Name the blood parasite species.
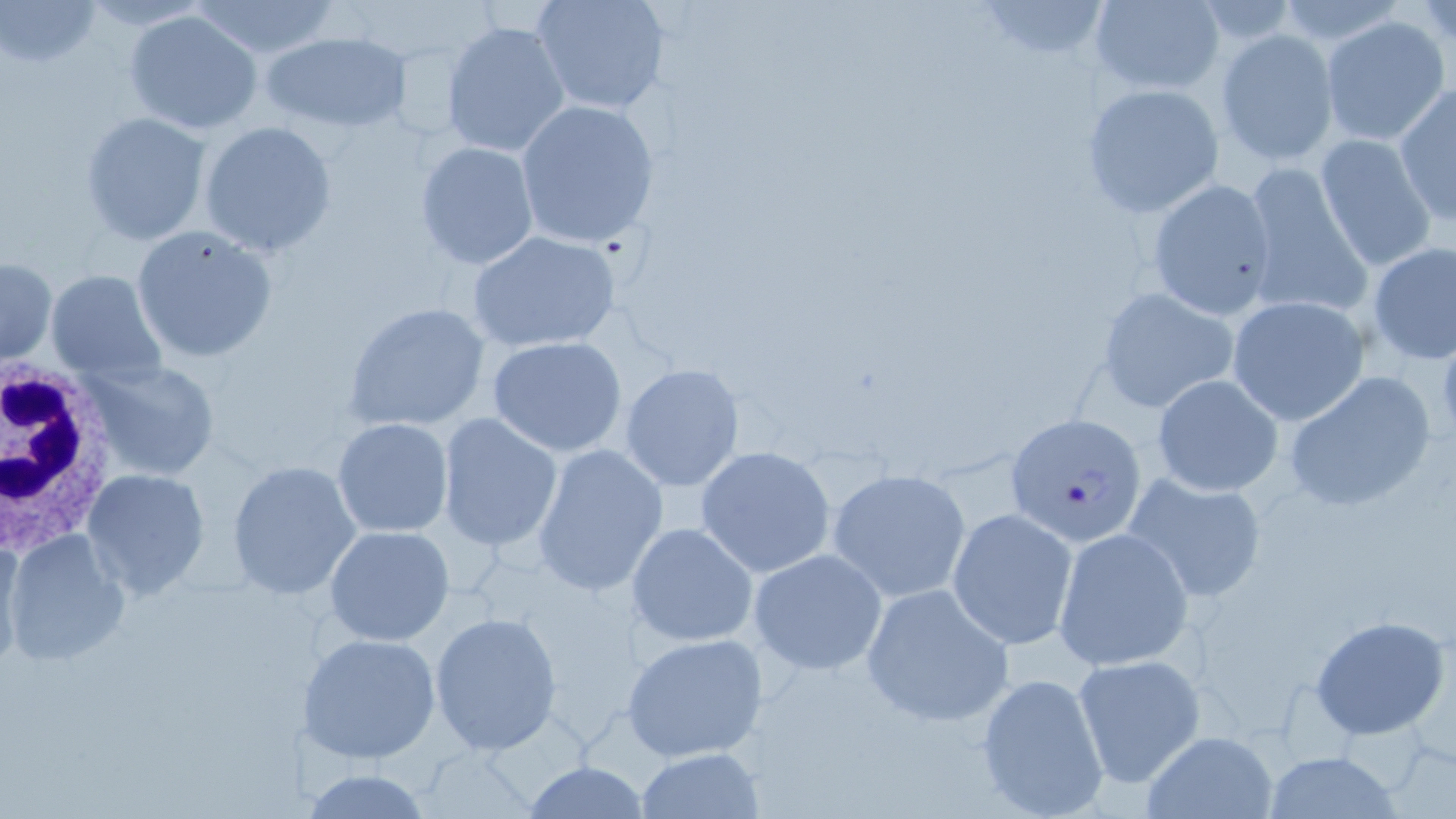
Plasmodium falciparum.

Approximate bounding boxes as (x1,y1)-(x2,y2) corner pairs in pixels. White blood cell locations: (0,358)-(121,560). Uninfected red blood cell locations: (78,0)-(214,30), (531,0)-(670,116), (1089,0)-(1225,95), (2,1)-(104,71), (190,1)-(339,60), (969,1)-(1116,64), (123,9)-(265,135), (1322,16)-(1450,145), (440,20)-(571,160), (1215,30)-(1340,166), (262,31)-(411,133), (1393,84)-(1455,226), (1083,85)-(1224,217), (515,99)-(661,248), (79,111)-(211,246), (198,120)-(338,257), (1314,134)-(1438,272), (414,141)-(542,269), (1240,162)-(1373,321), (1146,178)-(1279,320), (131,225)-(278,363), (466,230)-(625,353), (1366,242)-(1456,364), (1,255)-(57,365), (45,269)-(166,383), (1095,285)-(1242,415), (1226,295)-(1369,426), (345,301)-(492,432), (486,336)-(629,457), (83,358)-(220,482), (619,363)-(743,492), (1281,370)-(1439,514), (1152,374)-(1285,497), (436,412)-(563,552), (333,418)-(452,537), (532,443)-(669,599), (694,446)-(840,579), (226,460)-(363,599), (826,467)-(971,602), (82,468)-(212,598), (1122,472)-(1269,606), (948,509)-(1078,651), (627,522)-(759,648), (324,525)-(454,646), (1052,526)-(1193,671), (3,529)-(130,666), (0,531)-(24,671), (749,548)-(888,675), (860,582)-(1016,728), (429,612)-(563,753), (1309,614)-(1451,741), (300,632)-(442,764), (620,632)-(770,764), (1072,655)-(1205,787), (974,672)-(1111,817), (1143,732)-(1277,818), (634,747)-(765,818), (1262,751)-(1402,818), (520,762)-(654,819), (303,766)-(435,818). Plasmodium falciparum-infected red blood cell locations: (1007,412)-(1148,545). Image is 1456×819 pixels. May-Grünwald-Giemsa stain. One field of a larger specimen. 1000x magnification. Thin blood film. Light microscopy.